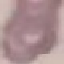

malaria status = uninfected
preparation = thin blood smear
capture = smartphone through the microscope eyepiece
image type = cell patch, automatically extracted from a larger field of view and resized to 64 × 64 pixels
stain = Giemsa